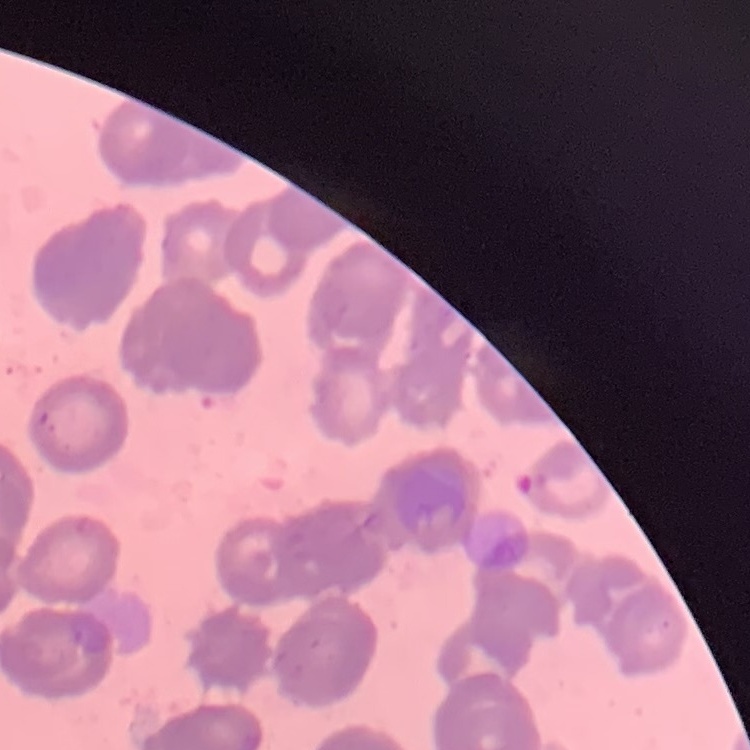

red blood cell morphology = rouleaux formation
preparation = thin peripheral smear
image type = square crop of a larger photomicrograph
stain = Field's or Giemsa